Locate every blood parasite and identify its species.
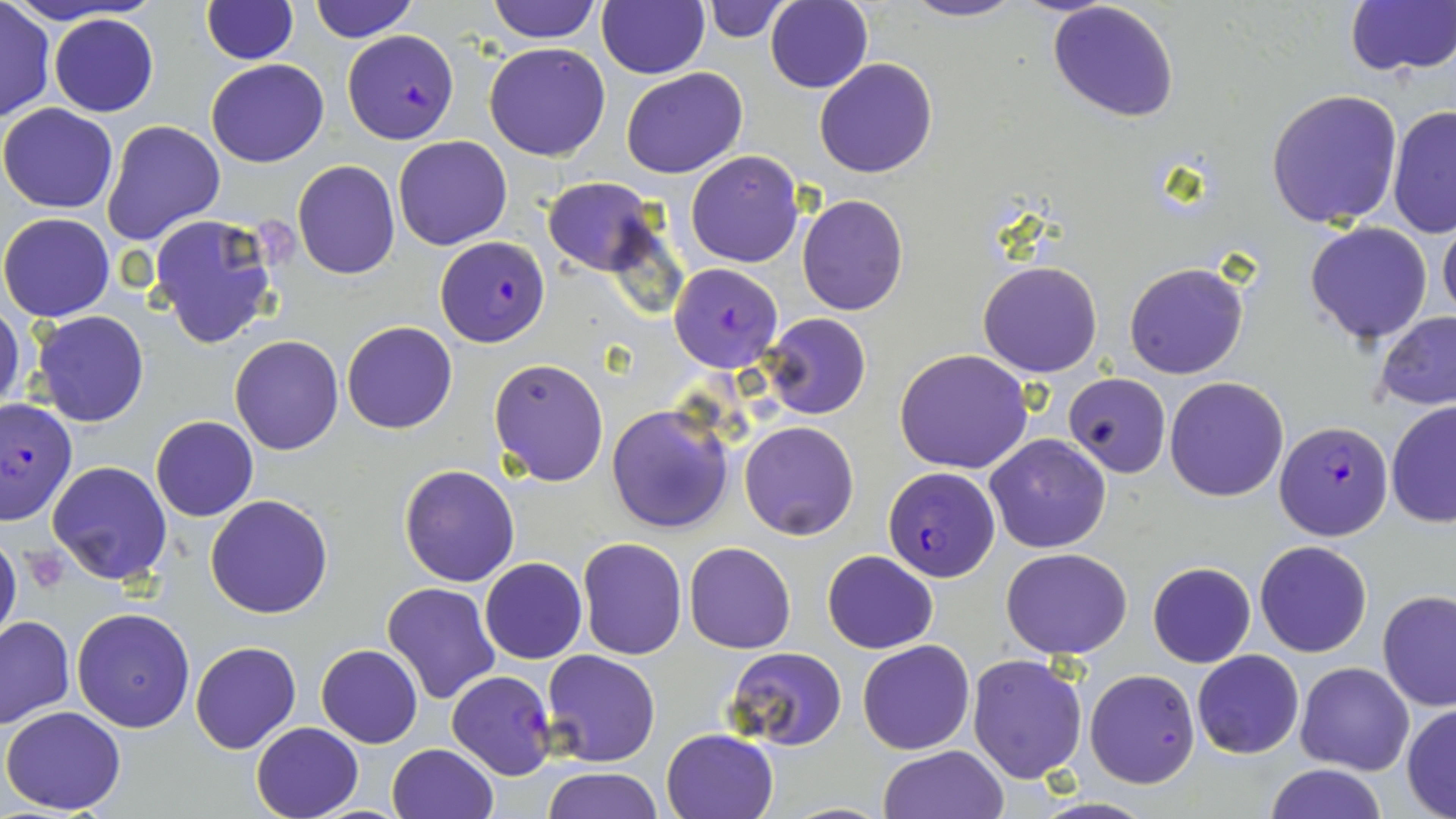

Approximate bounding boxes as (x1, y1, x2, y2) in pixels.
Plasmodium falciparum-infected red blood cells: (343, 30, 459, 143), (437, 235, 548, 346), (668, 263, 782, 372), (0, 396, 78, 525), (1274, 420, 1393, 540), (882, 469, 1000, 582), (447, 669, 557, 779).
No Plasmodium ovale, Plasmodium malariae, Plasmodium vivax, Babesia divergens, or Trypanosoma brucei observed.

slide_level_diagnosis: Plasmodium falciparum
stain: May-Grünwald-Giemsa
magnification: 1000x
modality: optical microscopy
field_of_view: one of a larger specimen
uninfected_red_blood_cell_locations: 'approximate bounding boxes as (x1, y1, x2, y2) in pixels: (201, 0, 297, 65), (310, 0, 418, 42), (488, 0, 600, 43), (595, 0, 709, 78), (900, 0, 1026, 23), (0, 1, 55, 120), (700, 1, 791, 42), (765, 1, 873, 91), (1048, 1, 1181, 123), (1343, 2, 1456, 79), (49, 14, 158, 117), (485, 42, 611, 161), (813, 56, 938, 179), (205, 58, 328, 167), (621, 66, 748, 177), (1264, 89, 1404, 230), (1386, 102, 1456, 240), (0, 103, 118, 213), (100, 119, 226, 247), (393, 135, 512, 249), (685, 150, 805, 268), (292, 159, 402, 280), (541, 177, 659, 275), (797, 195, 909, 316), (0, 212, 115, 321), (146, 212, 283, 351), (1438, 213, 1456, 326), (1304, 221, 1434, 346), (977, 260, 1103, 378), (1122, 260, 1250, 380), (0, 307, 26, 415), (28, 311, 150, 429), (1374, 311, 1456, 411), (761, 313, 871, 419), (341, 320, 458, 434), (228, 335, 345, 455), (895, 348, 1033, 473), (488, 356, 610, 487), (1064, 373, 1169, 477), (1164, 376, 1290, 501), (1385, 402, 1456, 528), (606, 403, 734, 534), (150, 416, 258, 522), (739, 420, 859, 540), (985, 434, 1112, 553), (45, 460, 172, 586), (398, 463, 521, 586), (204, 494, 335, 619), (0, 529, 22, 651), (577, 538, 687, 659), (1254, 540, 1372, 657), (683, 541, 797, 653), (1002, 548, 1131, 659), (822, 550, 938, 654), (480, 556, 587, 664), (1277, 558, 1392, 724), (1147, 562, 1256, 667), (381, 582, 500, 705), (1377, 589, 1456, 711), (72, 607, 195, 732), (0, 616, 75, 730), (190, 639, 301, 754), (857, 639, 975, 755), (316, 644, 423, 748), (723, 646, 848, 749), (1192, 649, 1304, 758), (541, 650, 662, 767), (967, 654, 1088, 783), (1295, 662, 1415, 774), (1085, 669, 1199, 788), (1402, 703, 1456, 818), (2, 706, 128, 815), (249, 721, 364, 819), (661, 728, 779, 819), (386, 743, 499, 819), (878, 745, 1011, 819), (1264, 764, 1387, 819), (541, 766, 661, 819)'
platelet_locations: 'approximate bounding boxes as (x1, y1, x2, y2) in pixels: (22, 547, 69, 592)'
preparation: thin blood film
image_size: 1456×819 pixels